Identify the blood parasite species.
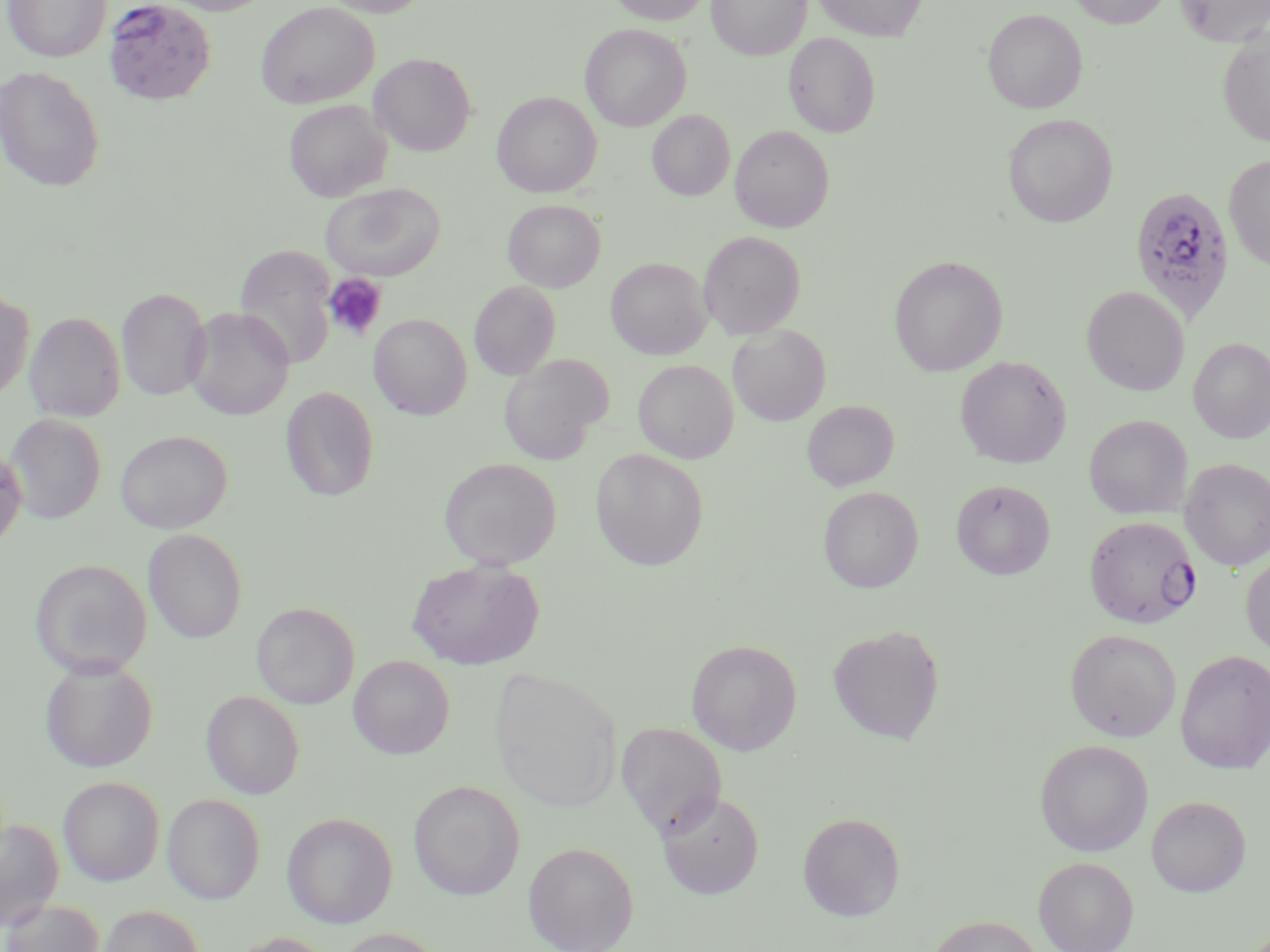
Plasmodium falciparum.

Summary:
  - Coordinate format: approximate bounding boxes as named x1/y1/x2/y2 corners in pixels
  - Uninfected red blood cell locations: (x1=1, y1=0, x2=111, y2=62), (x1=160, y1=0, x2=276, y2=15), (x1=319, y1=0, x2=432, y2=17), (x1=608, y1=0, x2=711, y2=25), (x1=707, y1=0, x2=810, y2=60), (x1=811, y1=0, x2=927, y2=41), (x1=1066, y1=0, x2=1173, y2=27), (x1=1174, y1=0, x2=1270, y2=47), (x1=256, y1=2, x2=379, y2=108), (x1=982, y1=8, x2=1087, y2=113), (x1=580, y1=24, x2=691, y2=131), (x1=1217, y1=31, x2=1270, y2=147), (x1=784, y1=32, x2=880, y2=137), (x1=370, y1=53, x2=475, y2=156), (x1=0, y1=65, x2=106, y2=192), (x1=492, y1=92, x2=601, y2=197), (x1=284, y1=99, x2=391, y2=202), (x1=647, y1=110, x2=734, y2=200), (x1=1003, y1=114, x2=1117, y2=227), (x1=730, y1=124, x2=834, y2=232), (x1=1223, y1=153, x2=1270, y2=272), (x1=321, y1=183, x2=445, y2=281), (x1=503, y1=200, x2=605, y2=292), (x1=698, y1=230, x2=805, y2=338), (x1=236, y1=247, x2=336, y2=370), (x1=889, y1=255, x2=1007, y2=376), (x1=606, y1=257, x2=711, y2=359), (x1=469, y1=280, x2=561, y2=380), (x1=1082, y1=285, x2=1189, y2=395), (x1=116, y1=287, x2=211, y2=401), (x1=0, y1=289, x2=34, y2=400), (x1=185, y1=307, x2=294, y2=420), (x1=24, y1=311, x2=126, y2=422), (x1=370, y1=314, x2=472, y2=419), (x1=727, y1=324, x2=830, y2=426), (x1=1188, y1=337, x2=1270, y2=443), (x1=498, y1=355, x2=612, y2=465), (x1=955, y1=356, x2=1072, y2=468), (x1=633, y1=359, x2=739, y2=463), (x1=280, y1=386, x2=379, y2=502), (x1=802, y1=400, x2=899, y2=491), (x1=5, y1=414, x2=106, y2=524), (x1=1084, y1=414, x2=1192, y2=519), (x1=115, y1=430, x2=232, y2=533), (x1=0, y1=444, x2=27, y2=551), (x1=591, y1=448, x2=709, y2=571), (x1=439, y1=457, x2=561, y2=570), (x1=1180, y1=458, x2=1270, y2=571), (x1=951, y1=479, x2=1055, y2=580), (x1=818, y1=486, x2=923, y2=592), (x1=143, y1=528, x2=248, y2=644), (x1=1241, y1=551, x2=1270, y2=659), (x1=29, y1=558, x2=152, y2=678), (x1=407, y1=559, x2=544, y2=670), (x1=251, y1=602, x2=360, y2=709), (x1=827, y1=625, x2=944, y2=744), (x1=1065, y1=628, x2=1182, y2=741), (x1=686, y1=639, x2=802, y2=755), (x1=1175, y1=649, x2=1270, y2=773), (x1=348, y1=655, x2=454, y2=759), (x1=39, y1=659, x2=158, y2=772), (x1=490, y1=666, x2=624, y2=812), (x1=201, y1=691, x2=304, y2=798), (x1=616, y1=722, x2=727, y2=835), (x1=1034, y1=739, x2=1153, y2=856), (x1=57, y1=776, x2=164, y2=886), (x1=408, y1=780, x2=525, y2=900), (x1=656, y1=791, x2=764, y2=900), (x1=162, y1=793, x2=265, y2=904), (x1=1146, y1=795, x2=1251, y2=897), (x1=798, y1=811, x2=905, y2=921), (x1=281, y1=812, x2=398, y2=928), (x1=0, y1=817, x2=64, y2=931), (x1=523, y1=841, x2=639, y2=952), (x1=1033, y1=856, x2=1138, y2=952), (x1=1, y1=899, x2=105, y2=952), (x1=98, y1=904, x2=204, y2=952), (x1=926, y1=914, x2=1042, y2=952), (x1=332, y1=927, x2=446, y2=952), (x1=226, y1=932, x2=338, y2=952)
  - Platelet locations: (x1=323, y1=274, x2=387, y2=342)
  - Plasmodium falciparum-infected red blood cell locations: (x1=103, y1=3, x2=217, y2=109), (x1=1126, y1=186, x2=1232, y2=323), (x1=1092, y1=519, x2=1207, y2=632)
  - Modality: light microscopy
  - Preparation: thin blood film
  - Field of view: single
  - Magnification: 1000x
  - Stain: May-Grünwald-Giemsa
  - Image size: 1270×952 pixels